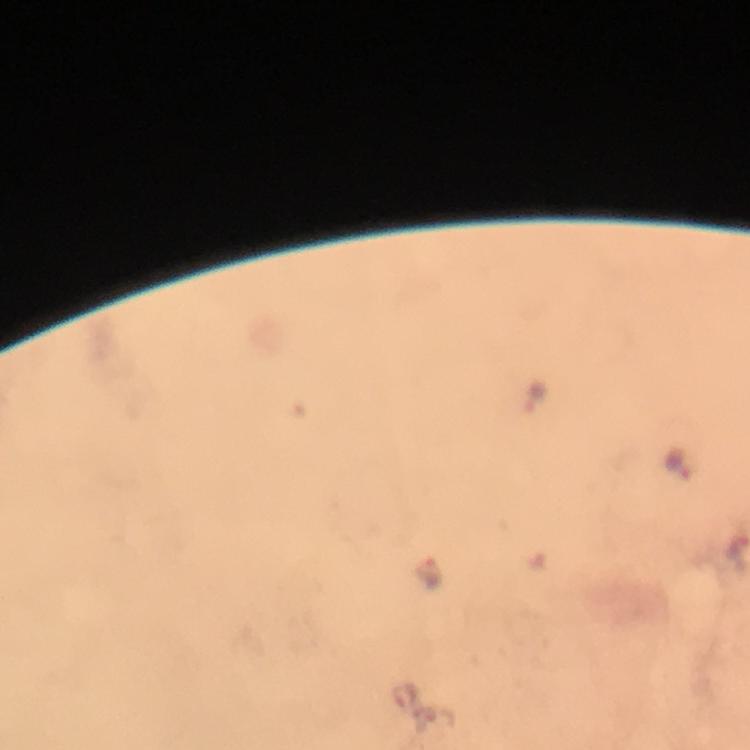
{
  "cropped_from": "one field of view",
  "preparation": "thick smear",
  "immersion_oil": "used",
  "capture": "smartphone camera through the microscope",
  "image_size": "750×750 pixels",
  "stain": "Giemsa",
  "malaria_parasite_locations": "approximate centers as [x, y] in pixels: [537, 396], [677, 467], [431, 571], [406, 699], [439, 718]",
  "magnification": "100x",
  "context": "from a diagnostic examination for malaria"
}